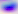

Photomicrograph. Toxoplasma gondii is seen. 400x magnification.